Locate and identify every blood parasite.
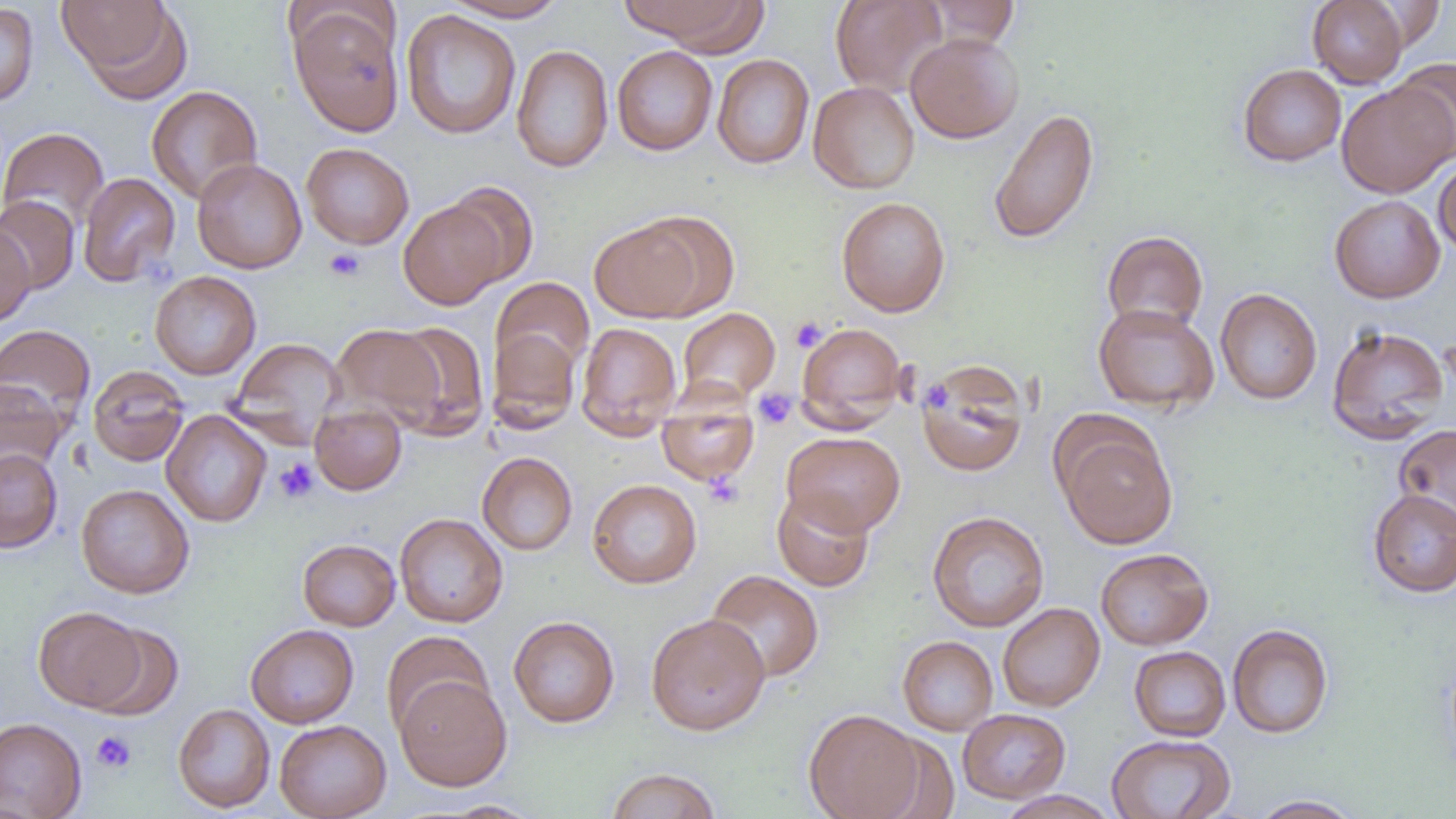

No blood parasites seen.

Summary:
  - Coordinate format: approximate bounding boxes as named x1/y1/x2/y2 corners in pixels
  - Uninfected red blood cell locations: (x1=59, y1=0, x2=188, y2=100), (x1=442, y1=0, x2=568, y2=22), (x1=619, y1=0, x2=768, y2=51), (x1=830, y1=0, x2=947, y2=96), (x1=923, y1=0, x2=1020, y2=48), (x1=1307, y1=0, x2=1409, y2=88), (x1=1365, y1=2, x2=1446, y2=51), (x1=0, y1=3, x2=39, y2=108), (x1=290, y1=7, x2=404, y2=136), (x1=400, y1=10, x2=522, y2=139), (x1=905, y1=32, x2=1024, y2=143), (x1=511, y1=44, x2=613, y2=173), (x1=612, y1=45, x2=718, y2=155), (x1=712, y1=54, x2=814, y2=169), (x1=1391, y1=58, x2=1456, y2=161), (x1=1237, y1=63, x2=1346, y2=166), (x1=808, y1=81, x2=919, y2=194), (x1=1336, y1=83, x2=1455, y2=198), (x1=146, y1=85, x2=263, y2=204), (x1=988, y1=108, x2=1099, y2=244), (x1=0, y1=127, x2=109, y2=233), (x1=301, y1=142, x2=414, y2=249), (x1=1433, y1=157, x2=1456, y2=259), (x1=192, y1=158, x2=307, y2=274), (x1=77, y1=172, x2=180, y2=287), (x1=441, y1=182, x2=539, y2=287), (x1=0, y1=195, x2=79, y2=293), (x1=1329, y1=195, x2=1445, y2=303), (x1=836, y1=196, x2=950, y2=317), (x1=398, y1=201, x2=506, y2=310), (x1=589, y1=218, x2=709, y2=322), (x1=0, y1=225, x2=35, y2=327), (x1=1102, y1=230, x2=1209, y2=334), (x1=150, y1=270, x2=261, y2=380), (x1=491, y1=277, x2=594, y2=383), (x1=1215, y1=288, x2=1322, y2=405), (x1=1093, y1=303, x2=1219, y2=413), (x1=678, y1=307, x2=779, y2=405), (x1=387, y1=321, x2=490, y2=438), (x1=488, y1=322, x2=584, y2=432), (x1=576, y1=322, x2=682, y2=437), (x1=796, y1=322, x2=908, y2=429), (x1=330, y1=323, x2=445, y2=427), (x1=0, y1=324, x2=95, y2=428), (x1=1326, y1=324, x2=1450, y2=444), (x1=230, y1=337, x2=347, y2=438), (x1=916, y1=360, x2=1030, y2=477), (x1=88, y1=365, x2=190, y2=467), (x1=0, y1=379, x2=68, y2=479), (x1=657, y1=395, x2=758, y2=487), (x1=309, y1=405, x2=407, y2=495), (x1=161, y1=410, x2=271, y2=527), (x1=1054, y1=420, x2=1178, y2=548), (x1=1394, y1=424, x2=1456, y2=531), (x1=782, y1=431, x2=905, y2=536), (x1=0, y1=448, x2=63, y2=552), (x1=477, y1=452, x2=577, y2=555), (x1=587, y1=479, x2=702, y2=588), (x1=76, y1=484, x2=195, y2=598), (x1=772, y1=488, x2=875, y2=591), (x1=1367, y1=489, x2=1456, y2=597), (x1=926, y1=511, x2=1050, y2=632), (x1=394, y1=513, x2=508, y2=628), (x1=298, y1=539, x2=400, y2=631), (x1=1095, y1=547, x2=1213, y2=650), (x1=706, y1=569, x2=824, y2=682), (x1=998, y1=603, x2=1104, y2=711), (x1=34, y1=606, x2=148, y2=712), (x1=646, y1=613, x2=770, y2=735), (x1=508, y1=615, x2=620, y2=728), (x1=88, y1=624, x2=184, y2=720), (x1=245, y1=624, x2=359, y2=728), (x1=1227, y1=624, x2=1334, y2=738), (x1=381, y1=630, x2=492, y2=735), (x1=897, y1=635, x2=998, y2=735), (x1=1129, y1=646, x2=1230, y2=741), (x1=395, y1=674, x2=512, y2=790), (x1=173, y1=703, x2=275, y2=813), (x1=804, y1=708, x2=923, y2=819), (x1=957, y1=709, x2=1070, y2=804), (x1=0, y1=717, x2=87, y2=818), (x1=274, y1=720, x2=391, y2=819), (x1=1106, y1=734, x2=1236, y2=818), (x1=604, y1=768, x2=722, y2=819), (x1=995, y1=790, x2=1119, y2=819), (x1=1249, y1=794, x2=1364, y2=818), (x1=440, y1=800, x2=543, y2=818)
  - Platelet locations: (x1=324, y1=248, x2=365, y2=281), (x1=789, y1=316, x2=827, y2=352), (x1=928, y1=380, x2=950, y2=414), (x1=753, y1=388, x2=797, y2=430), (x1=274, y1=458, x2=319, y2=504), (x1=703, y1=472, x2=745, y2=508), (x1=91, y1=730, x2=136, y2=774)
  - Slide-level diagnosis: no evidence of blood parasites
  - Magnification: 1000x
  - Image size: 1456×819 pixels
  - Preparation: thin blood smear
  - Modality: light microscopy
  - Field of view: one of a larger specimen